Outline each blood parasite and name the species.
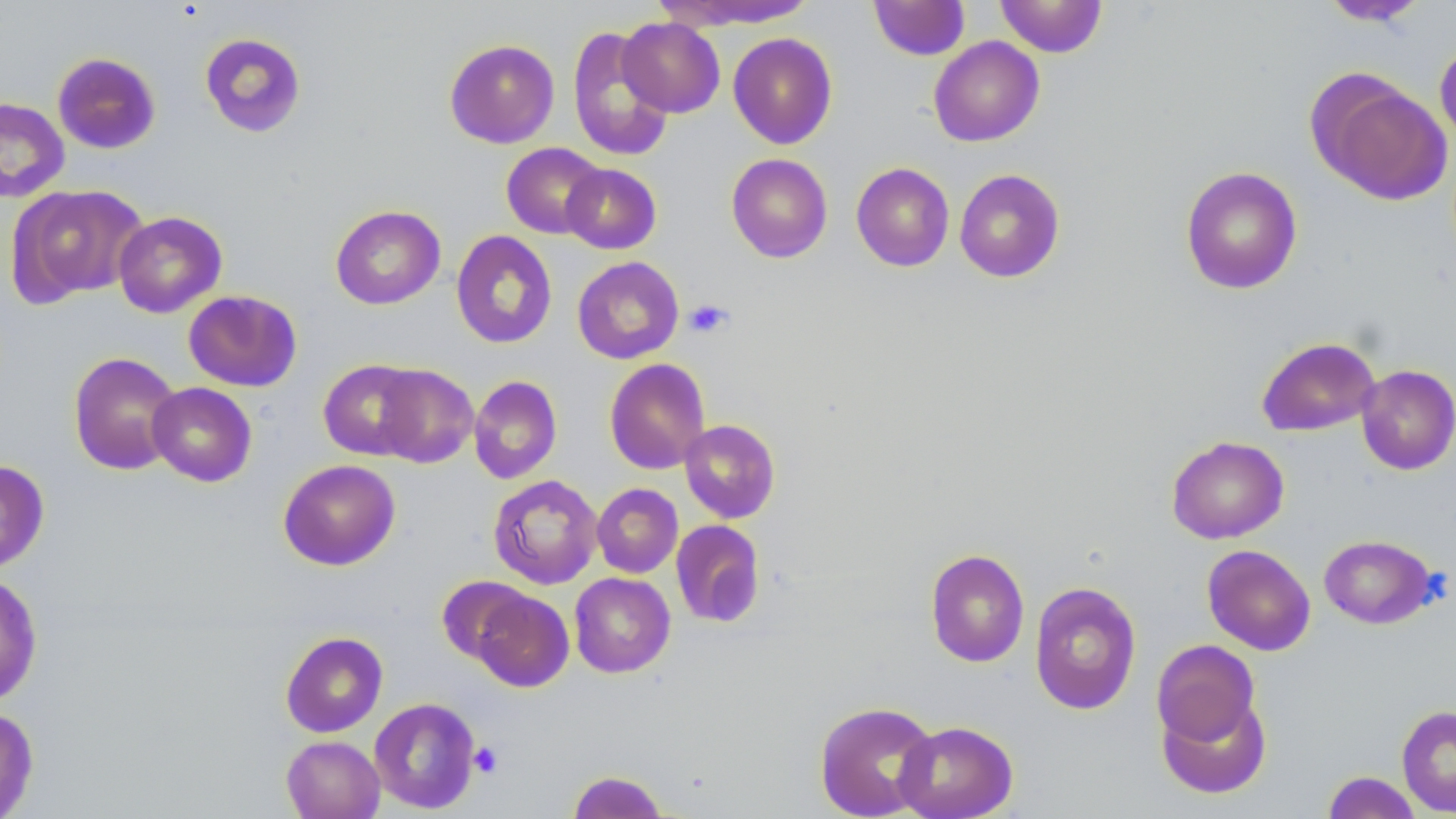

No blood parasites seen.

Summary:
  - Coordinate format: approximate bounding boxes as (x1,y1)-(x2,y2) corner pairs in pixels
  - Platelet locations: (683,299)-(734,338), (469,742)-(502,778)
  - Uninfected red blood cell locations: (995,0)-(1108,57), (1318,0)-(1430,26), (662,1)-(817,30), (869,1)-(970,60), (617,17)-(725,118), (567,26)-(674,162), (199,32)-(306,137), (727,32)-(838,149), (928,36)-(1045,146), (1435,38)-(1456,151), (444,39)-(560,148), (52,52)-(161,154), (1313,77)-(1452,206), (0,97)-(70,202), (501,143)-(606,239), (726,153)-(833,263), (851,162)-(954,271), (561,163)-(661,254), (1180,166)-(1303,295), (954,169)-(1066,283), (8,185)-(149,306), (330,205)-(446,309), (113,211)-(227,318), (451,230)-(557,349), (572,256)-(684,364), (183,289)-(302,392), (1256,337)-(1381,436), (68,351)-(182,476), (604,358)-(710,474), (318,359)-(426,460), (371,364)-(478,468), (1356,364)-(1456,475), (469,375)-(562,484), (147,382)-(257,487), (679,419)-(781,523), (1166,436)-(1289,544), (278,459)-(401,571), (0,460)-(50,572), (488,474)-(603,589), (592,483)-(683,578), (671,519)-(765,628), (1318,534)-(1439,629), (1202,544)-(1316,655), (925,548)-(1030,667), (569,572)-(675,677), (0,574)-(43,706), (437,576)-(534,664), (1029,581)-(1142,715), (471,589)-(574,692), (280,631)-(388,737), (1151,639)-(1261,749), (1157,690)-(1272,799), (814,700)-(939,819), (371,705)-(484,811), (1397,705)-(1456,816), (0,706)-(39,818), (894,720)-(1018,819), (281,735)-(385,819), (566,770)-(670,818), (1322,771)-(1422,818)
  - Slide-level diagnosis: no evidence of blood parasites
  - Preparation: thin blood smear
  - Modality: optical microscopy
  - Magnification: 1000x
  - Field of view: one of a larger specimen
  - Stain: May-Grünwald-Giemsa
  - Image size: 1456×819 pixels